Assess this cell for malaria.
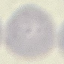

It is uninfected.

Cell patch, automatically extracted from a larger field of view and resized to 64 × 64 pixels. Giemsa stain. Acquired by smartphone through the microscope eyepiece. Thin blood film.